Classify this cell by malaria status.
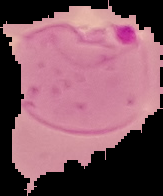

Parasitized.

Image is 163×196 pixels. The area outside the segmented cell region is set to black. From a thin blood smear.